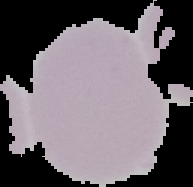
Result: no Plasmodium parasites detected. The area outside the segmented cell region is set to black. Image is 193×187 pixels. From a thin blood smear.